Outline each blood parasite and name the species.
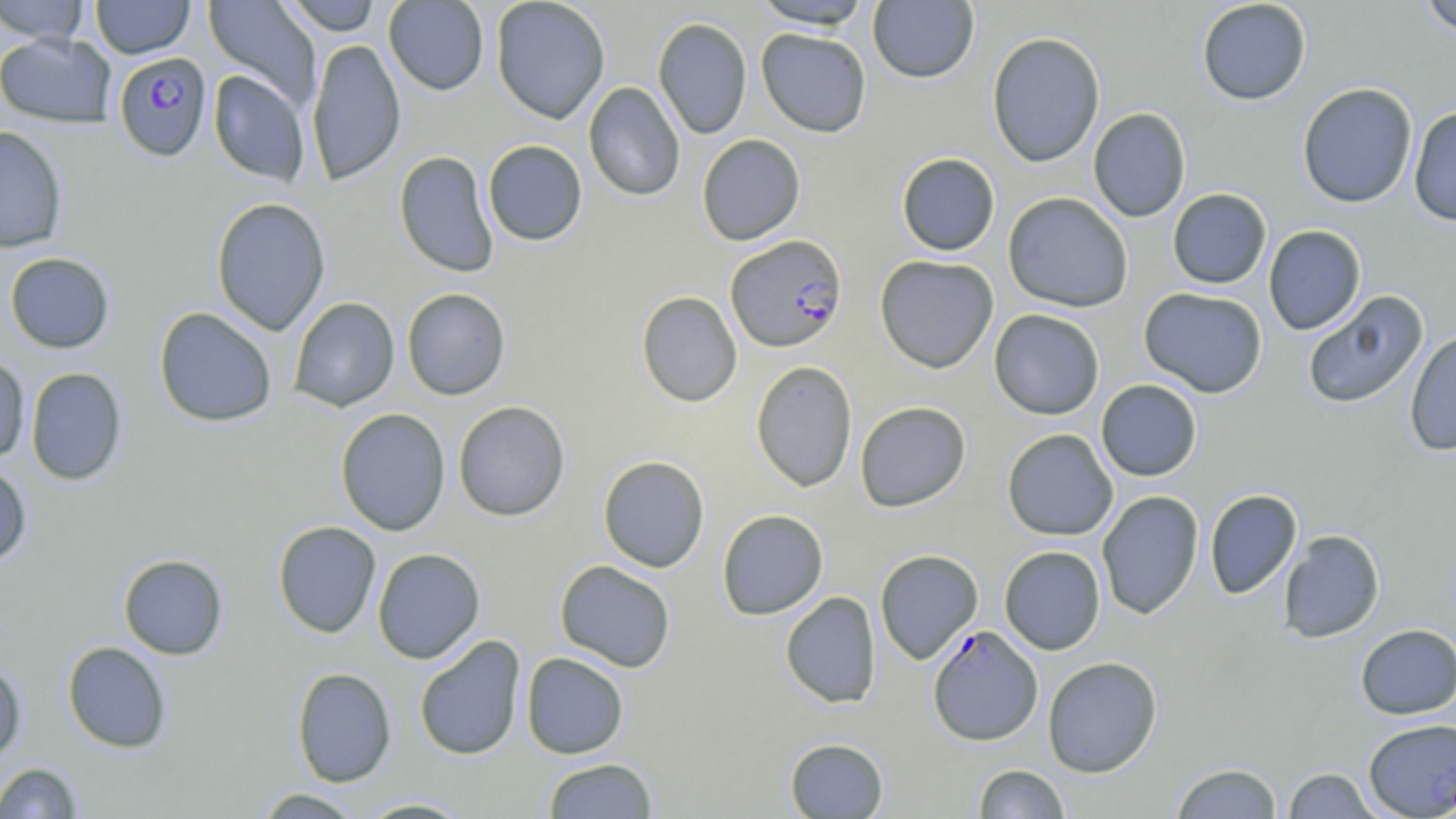

Approximate bounding boxes as named x1/y1/x2/y2 corners in pixels.
Plasmodium falciparum-infected red blood cells: (x1=114, y1=53, x2=212, y2=163), (x1=726, y1=234, x2=847, y2=352), (x1=927, y1=625, x2=1043, y2=747).
No Plasmodium ovale, Plasmodium malariae, Plasmodium vivax, Babesia divergens, or Trypanosoma brucei observed.

Uninfected red blood cell locations: (x1=0, y1=0, x2=91, y2=44), (x1=91, y1=0, x2=195, y2=59), (x1=203, y1=0, x2=322, y2=107), (x1=281, y1=0, x2=384, y2=36), (x1=384, y1=0, x2=489, y2=96), (x1=491, y1=0, x2=610, y2=124), (x1=751, y1=0, x2=874, y2=29), (x1=1196, y1=0, x2=1312, y2=105), (x1=1418, y1=0, x2=1456, y2=37), (x1=868, y1=1, x2=979, y2=84), (x1=653, y1=16, x2=752, y2=139), (x1=756, y1=28, x2=872, y2=137), (x1=986, y1=31, x2=1106, y2=168), (x1=0, y1=32, x2=117, y2=128), (x1=306, y1=38, x2=406, y2=186), (x1=209, y1=70, x2=310, y2=186), (x1=583, y1=81, x2=685, y2=201), (x1=1297, y1=83, x2=1418, y2=208), (x1=1407, y1=105, x2=1456, y2=227), (x1=1088, y1=107, x2=1191, y2=222), (x1=0, y1=126, x2=68, y2=252), (x1=696, y1=134, x2=806, y2=245), (x1=483, y1=140, x2=587, y2=246), (x1=394, y1=150, x2=499, y2=278), (x1=896, y1=152, x2=1000, y2=256), (x1=1167, y1=188, x2=1271, y2=289), (x1=1003, y1=192, x2=1134, y2=313), (x1=210, y1=197, x2=331, y2=336), (x1=1263, y1=225, x2=1366, y2=335), (x1=4, y1=252, x2=115, y2=354), (x1=874, y1=254, x2=999, y2=373), (x1=1138, y1=286, x2=1268, y2=398), (x1=402, y1=288, x2=511, y2=400), (x1=636, y1=290, x2=742, y2=407), (x1=1302, y1=290, x2=1429, y2=410), (x1=288, y1=297, x2=400, y2=412), (x1=153, y1=307, x2=277, y2=427), (x1=988, y1=309, x2=1105, y2=420), (x1=1404, y1=330, x2=1456, y2=456), (x1=0, y1=354, x2=30, y2=463), (x1=751, y1=360, x2=858, y2=492), (x1=25, y1=367, x2=127, y2=485), (x1=1095, y1=379, x2=1203, y2=481), (x1=453, y1=400, x2=570, y2=522), (x1=854, y1=400, x2=972, y2=512), (x1=335, y1=408, x2=451, y2=536), (x1=1002, y1=428, x2=1118, y2=541), (x1=598, y1=455, x2=710, y2=572), (x1=0, y1=462, x2=32, y2=567), (x1=1204, y1=488, x2=1302, y2=599), (x1=1096, y1=490, x2=1204, y2=620), (x1=716, y1=509, x2=829, y2=620), (x1=272, y1=520, x2=381, y2=638), (x1=1278, y1=529, x2=1385, y2=643), (x1=999, y1=545, x2=1106, y2=655), (x1=372, y1=548, x2=485, y2=664), (x1=874, y1=549, x2=983, y2=665), (x1=118, y1=554, x2=229, y2=659), (x1=555, y1=560, x2=676, y2=672), (x1=780, y1=591, x2=881, y2=708), (x1=1355, y1=624, x2=1456, y2=719), (x1=414, y1=634, x2=527, y2=761), (x1=62, y1=641, x2=172, y2=753), (x1=521, y1=652, x2=629, y2=759), (x1=1042, y1=656, x2=1163, y2=778), (x1=0, y1=659, x2=27, y2=764), (x1=291, y1=666, x2=396, y2=787), (x1=1363, y1=719, x2=1456, y2=815), (x1=784, y1=737, x2=889, y2=818), (x1=542, y1=758, x2=658, y2=818), (x1=1, y1=762, x2=83, y2=819), (x1=1170, y1=762, x2=1283, y2=818), (x1=973, y1=764, x2=1070, y2=819), (x1=1282, y1=767, x2=1383, y2=818), (x1=252, y1=787, x2=366, y2=818), (x1=354, y1=797, x2=476, y2=818). Slide-level diagnosis: Plasmodium falciparum. May-Grünwald-Giemsa-stained preparation. Optical microscopy. One field of a larger specimen. Captured at 1000x magnification. Image is 1456×819 pixels. Thin blood smear.